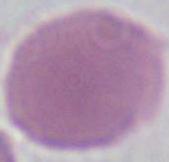
identification: erythrocyte
magnification: 1000x
modality: photomicrograph